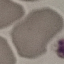

{
  "malaria_status": "uninfected",
  "capture": "smartphone through the microscope eyepiece",
  "stain": "Giemsa",
  "preparation": "thin blood film",
  "image_type": "cell patch, automatically extracted from a larger field of view and resized to 64 × 64 pixels"
}